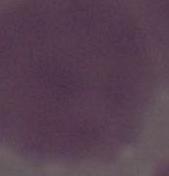

magnification = 1000x
identification = erythrocyte
modality = photomicrograph